Locate every Plasmodium parasite and every leukocyte.
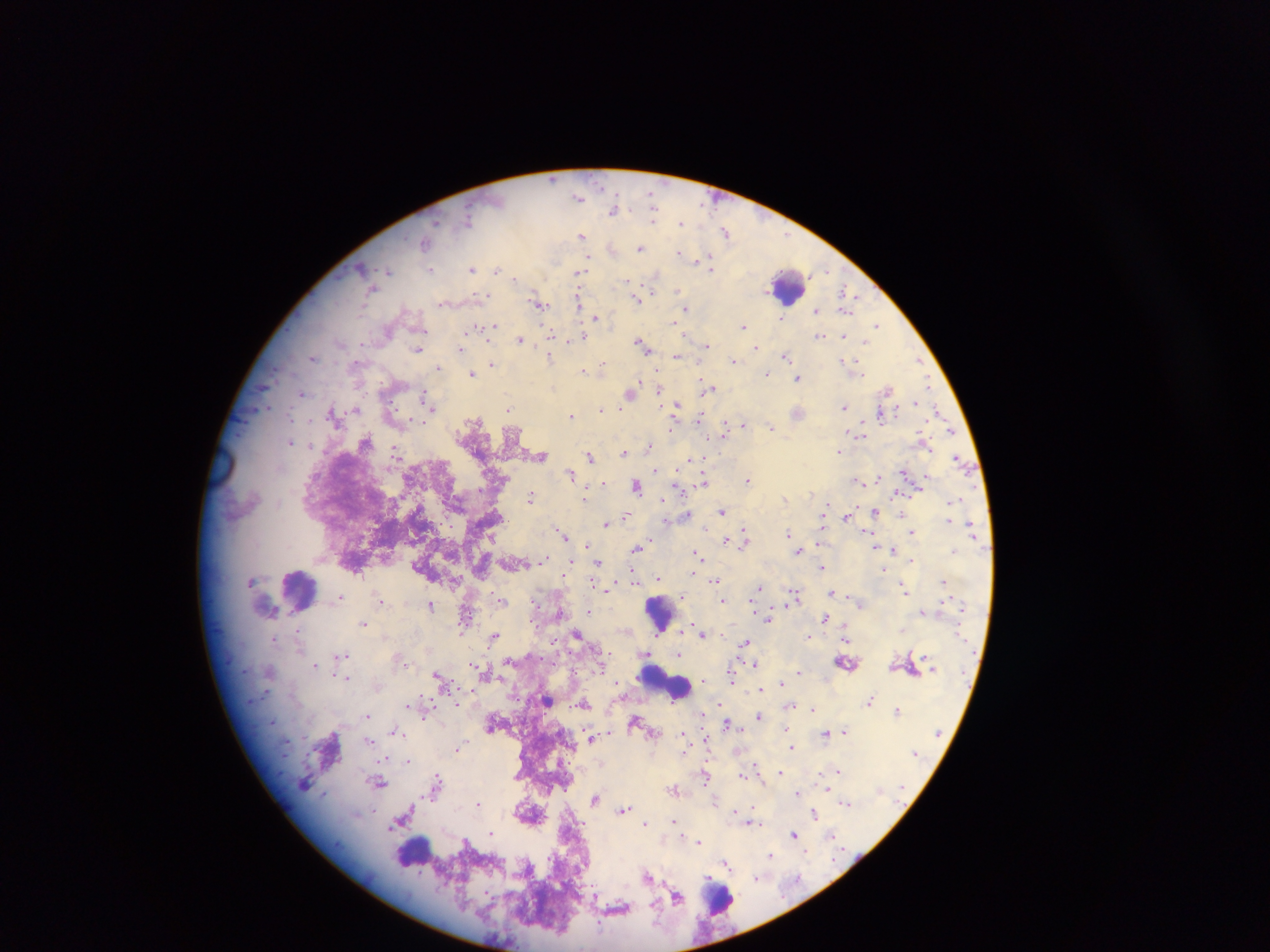
Approximate centers as {x, y} in pixels.
Plasmodium parasites: {651, 196}, {579, 197}, {613, 211}, {468, 220}, {653, 220}, {681, 223}, {726, 233}, {582, 235}, {424, 243}, {611, 247}, {641, 248}, {679, 252}, {587, 258}, {698, 259}, {711, 268}, {472, 269}, {429, 270}, {496, 270}, {387, 271}, {579, 273}, {655, 274}, {515, 278}, {628, 281}, {678, 291}, {844, 293}, {486, 295}, {637, 299}, {579, 301}, {539, 305}, {685, 308}, {817, 310}, {846, 310}, {596, 317}, {782, 318}, {675, 322}, {876, 325}, {492, 326}, {744, 327}, {476, 329}, {485, 329}, {551, 335}, {819, 335}, {845, 336}, {583, 338}, {521, 341}, {865, 343}, {706, 345}, {644, 346}, {460, 348}, {756, 348}, {418, 349}, {785, 355}, {550, 356}, {676, 356}, {313, 357}, {919, 359}, {733, 360}, {849, 361}, {491, 363}, {602, 365}, {438, 367}, {583, 370}, {472, 374}, {767, 375}, {798, 378}, {927, 385}, {263, 386}, {709, 388}, {659, 389}, {887, 390}, {302, 393}, {630, 393}, {424, 398}, {915, 401}, {428, 404}, {676, 406}, {844, 407}, {266, 408}, {433, 408}, {508, 408}, {602, 409}, {937, 409}, {355, 410}, {798, 413}, {881, 414}, {571, 415}, {699, 419}, {743, 424}, {771, 426}, {724, 428}, {950, 429}, {859, 433}, {365, 441}, {290, 442}, {649, 446}, {395, 450}, {625, 452}, {838, 452}, {541, 456}, {589, 457}, {691, 459}, {959, 461}, {655, 470}, {571, 473}, {879, 477}, {748, 479}, {856, 479}, {704, 481}, {603, 483}, {637, 486}, {531, 495}, {585, 498}, {954, 501}, {826, 504}, {723, 511}, {875, 511}, {687, 515}, {626, 516}, {847, 516}, {665, 520}, {606, 524}, {912, 531}, {563, 533}, {788, 533}, {866, 533}, {745, 536}, {726, 540}, {745, 542}, {586, 544}, {636, 548}, {799, 550}, {893, 550}, {697, 553}, {543, 560}, {912, 560}, {598, 562}, {570, 564}, {822, 567}, {883, 569}, {694, 574}, {658, 579}, {943, 580}, {715, 581}, {759, 588}, {606, 589}, {906, 591}, {832, 592}, {795, 595}, {682, 596}, {340, 597}, {381, 600}, {722, 600}, {502, 601}, {430, 605}, {588, 611}, {921, 613}, {465, 614}, {825, 617}, {768, 619}, {364, 622}, {699, 630}, {902, 630}, {661, 632}, {578, 634}, {702, 634}, {494, 637}, {808, 637}, {845, 638}, {746, 643}, {646, 654}, {679, 654}, {342, 655}, {847, 663}, {756, 664}, {315, 665}, {799, 672}, {438, 675}, {346, 678}, {704, 679}, {732, 679}, {781, 683}, {760, 690}, {869, 700}, {548, 701}, {583, 703}, {410, 704}, {791, 705}, {811, 709}, {897, 710}, {368, 715}, {759, 716}, {728, 723}, {786, 729}, {395, 731}, {844, 731}, {825, 733}, {683, 735}, {590, 737}, {369, 742}, {459, 747}, {792, 747}, {407, 760}, {756, 765}, {780, 772}, {838, 772}, {742, 775}, {706, 777}, {437, 779}, {379, 783}, {674, 789}, {797, 793}, {595, 798}, {478, 803}, {847, 803}, {624, 810}, {735, 811}, {814, 814}, {674, 821}, {645, 823}, {753, 823}, {400, 824}, {393, 826}, {492, 834}, {831, 834}, {794, 835}, {699, 842}, {770, 855}, {726, 864}, {648, 875}, {755, 878}, {677, 897}.
Leukocytes: {788, 287}, {301, 587}, {660, 607}, {653, 677}, {681, 689}, {414, 857}, {722, 899}.

Collected in Ghana. One field of view. Thick blood film. Mobile-phone photograph taken through the microscope. Image is 1270×952 pixels.